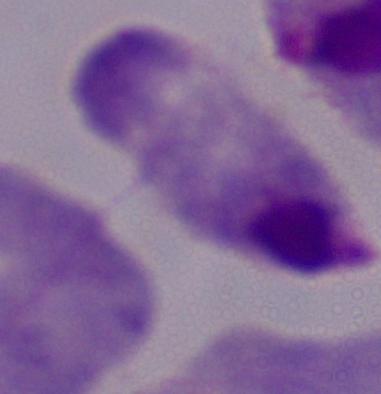

Summary:
  - Identification: trichomonad
  - Magnification: 1000x
  - Modality: micrograph